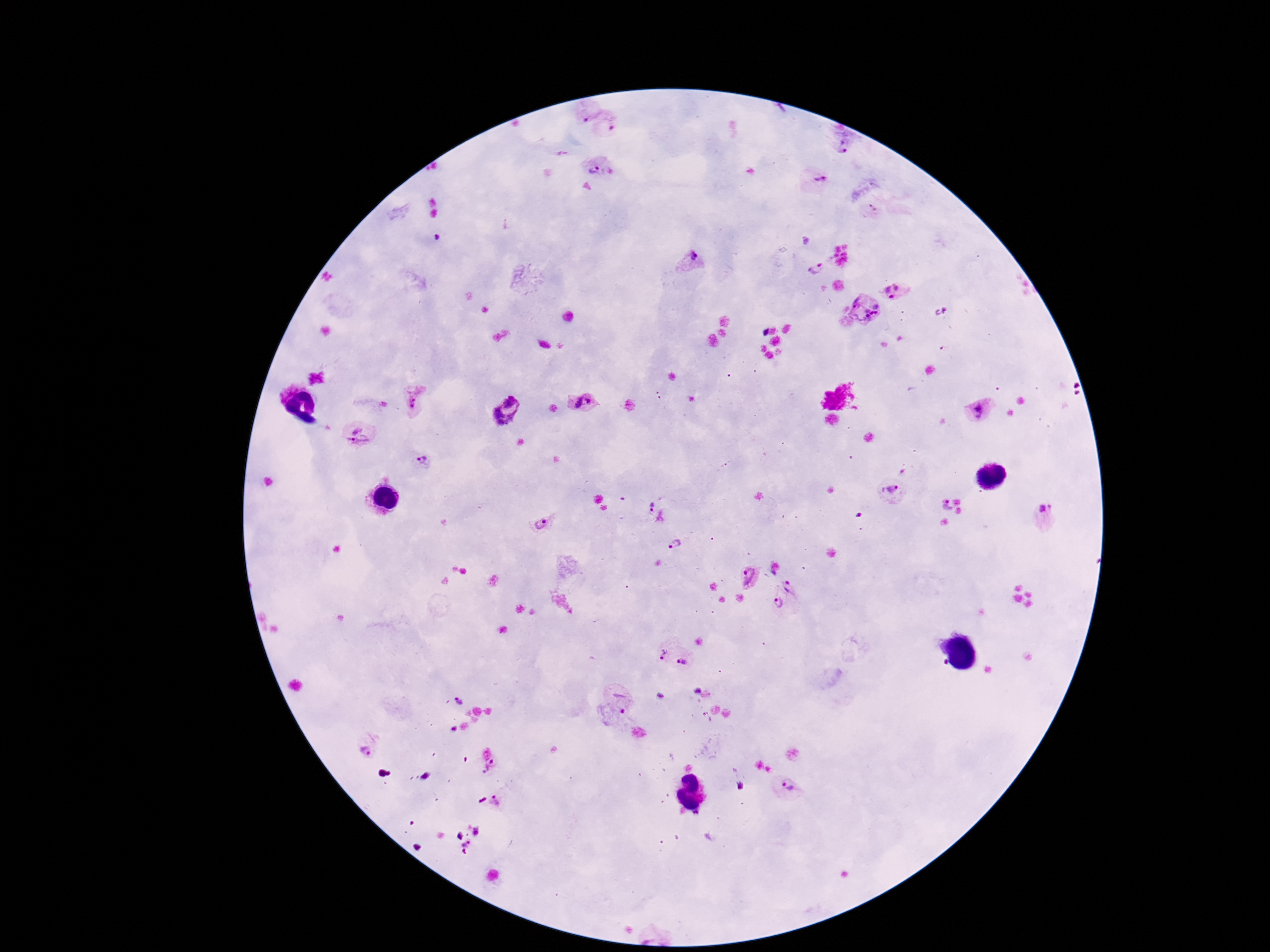

Approximate centers as (x, y) in pixels.
Summary:
  - Plasmodium parasite locations: (585, 107), (614, 129), (845, 142), (600, 169), (818, 180), (873, 210), (690, 261), (816, 267), (896, 291), (862, 313), (581, 399), (413, 401), (509, 409), (979, 411), (362, 437), (423, 458), (892, 490), (945, 505), (651, 507), (1045, 515), (661, 519), (542, 522), (675, 543), (749, 577), (792, 584), (775, 604), (663, 650), (686, 660), (616, 697), (458, 699), (364, 750), (496, 768), (787, 790), (496, 801)
  - Patient malaria status: infected
  - Magnification: 100x
  - Stain: Giemsa
  - Image size: 1270×952 pixels
  - Field of view: single
  - Capture: smartphone camera through the microscope eyepiece
  - Preparation: thick blood smear